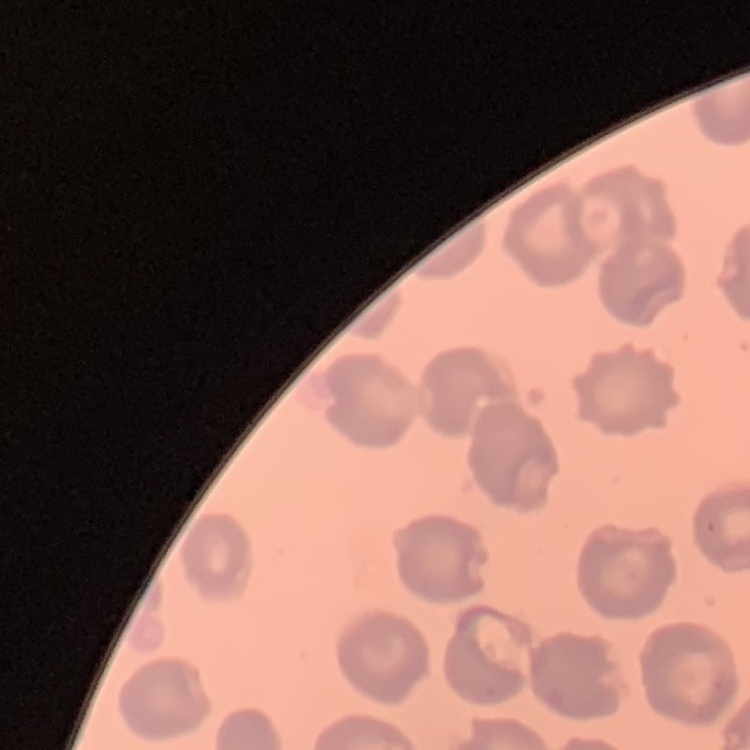

The erythrocytes exhibit no rouleaux formation. Thin blood smear. One tile cut from a larger photomicrograph. Field's or Giemsa stain.